Give the preparation type.
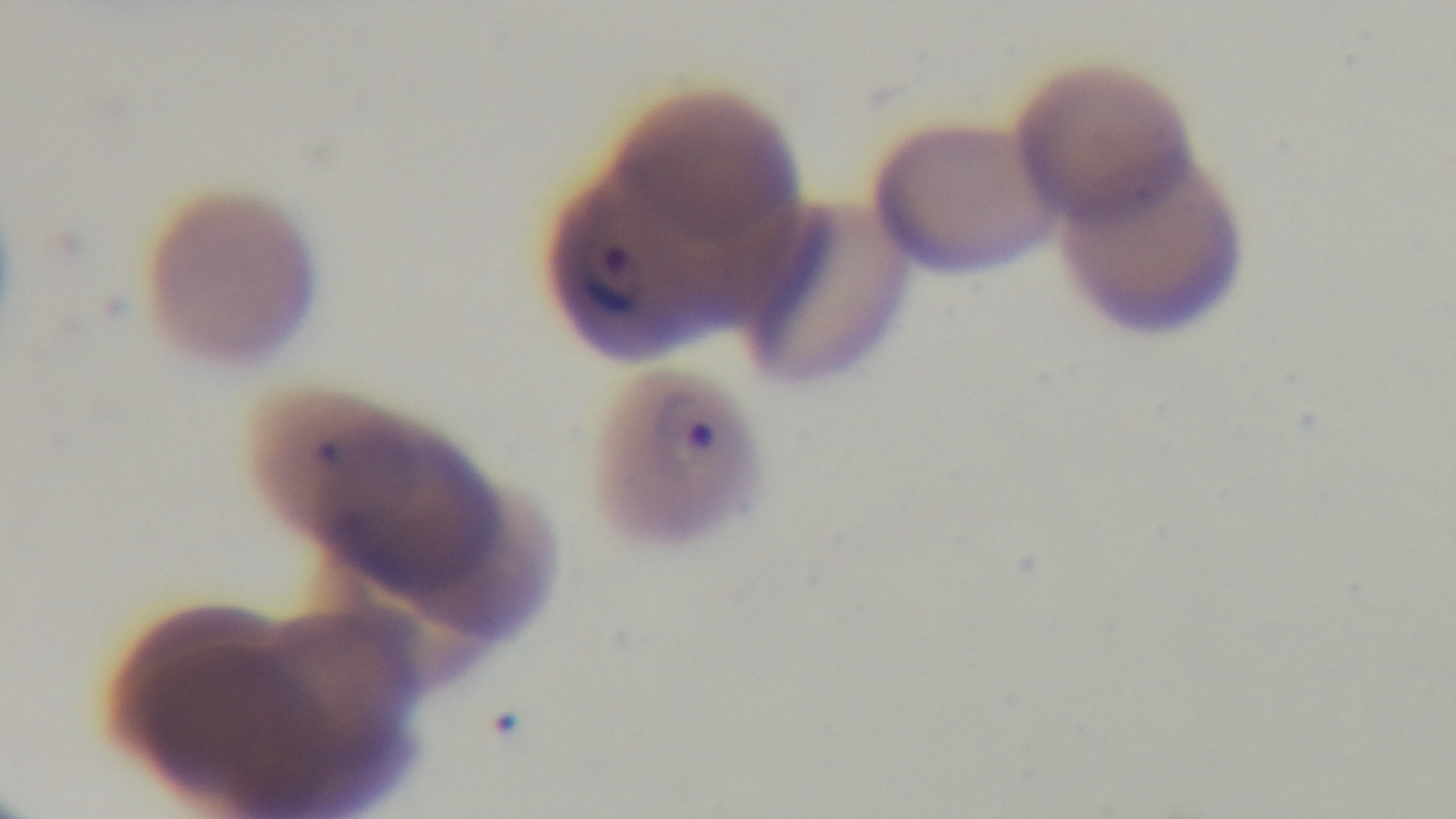

Thin.

Captured with a mounted 4K digital camera. Giemsa-stained. Malaria status: positive. Single field of view. Light microscopy. 100x oil-immersion objective.